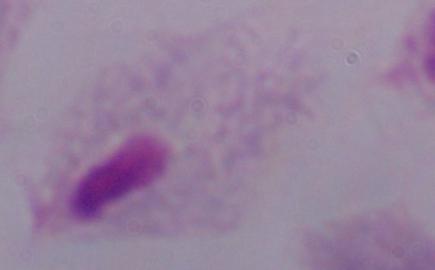
modality: micrograph
magnification: 1000x
identification: trichomonad